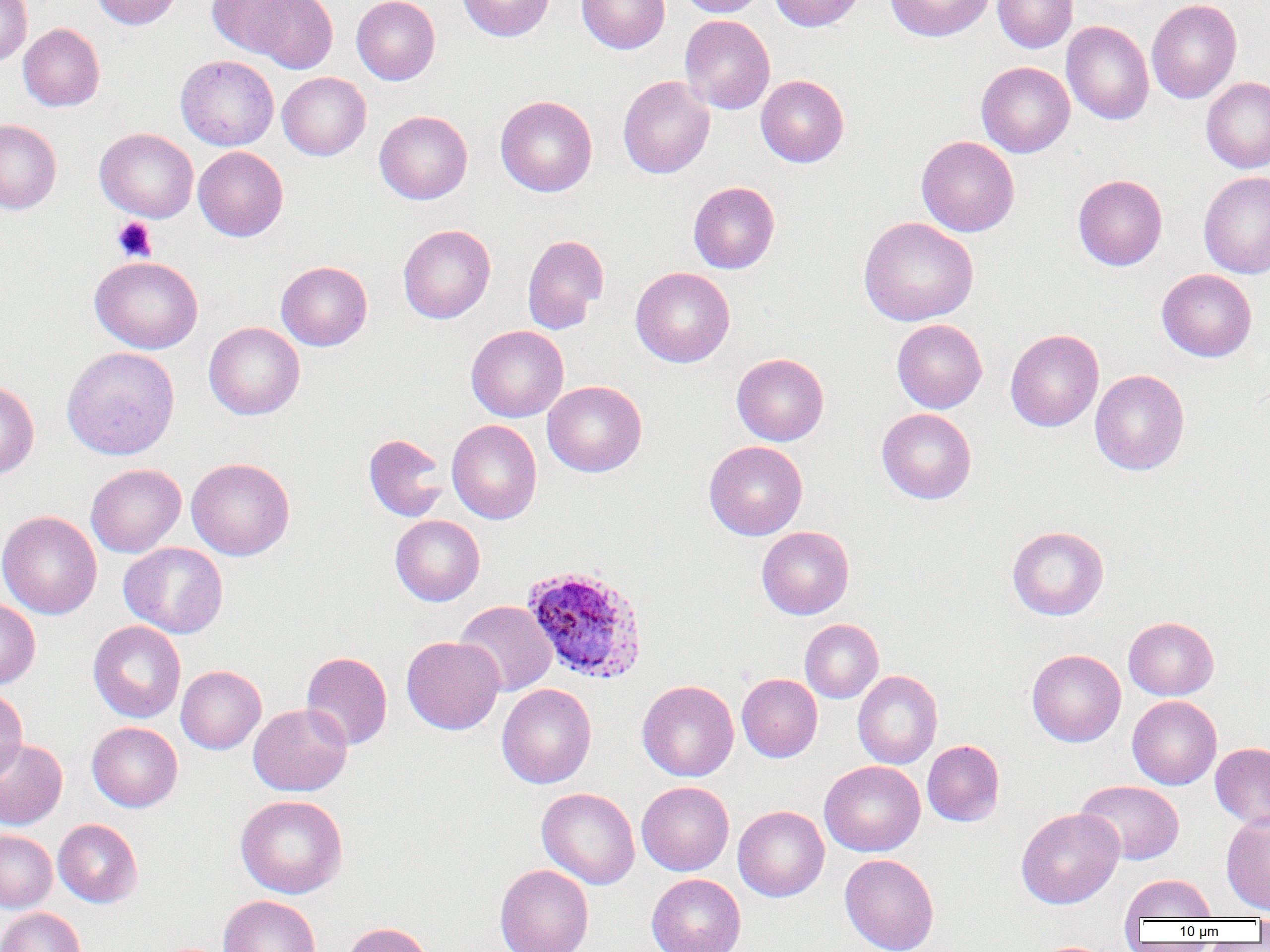
{
  "slide_level_diagnosis": "Plasmodium ovale",
  "preparation": "thin blood film",
  "plasmodium_ovale_infected_red_blood_cell_locations": "approximate bounding boxes as named x1/y1/x2/y2 corners in pixels: (x1=521, y1=564, x2=648, y2=684)",
  "magnification": "1000x",
  "platelet_locations": "approximate bounding boxes as named x1/y1/x2/y2 corners in pixels: (x1=112, y1=217, x2=157, y2=262)",
  "uninfected_red_blood_cell_locations": "approximate bounding boxes as named x1/y1/x2/y2 corners in pixels: (x1=0, y1=0, x2=32, y2=65), (x1=91, y1=0, x2=182, y2=29), (x1=206, y1=0, x2=302, y2=59), (x1=246, y1=0, x2=338, y2=74), (x1=352, y1=0, x2=440, y2=85), (x1=457, y1=0, x2=554, y2=41), (x1=576, y1=0, x2=669, y2=54), (x1=677, y1=0, x2=767, y2=17), (x1=768, y1=0, x2=866, y2=31), (x1=885, y1=0, x2=993, y2=42), (x1=993, y1=0, x2=1078, y2=53), (x1=1146, y1=0, x2=1242, y2=104), (x1=679, y1=15, x2=775, y2=114), (x1=1061, y1=20, x2=1154, y2=125), (x1=18, y1=23, x2=105, y2=111), (x1=175, y1=55, x2=279, y2=150), (x1=976, y1=61, x2=1075, y2=157), (x1=277, y1=72, x2=371, y2=160), (x1=756, y1=75, x2=849, y2=167), (x1=617, y1=76, x2=715, y2=178), (x1=1201, y1=77, x2=1270, y2=173), (x1=495, y1=95, x2=597, y2=197), (x1=375, y1=110, x2=473, y2=204), (x1=0, y1=119, x2=62, y2=214), (x1=95, y1=127, x2=198, y2=222), (x1=916, y1=136, x2=1020, y2=237), (x1=193, y1=146, x2=288, y2=241), (x1=1199, y1=171, x2=1270, y2=278), (x1=1073, y1=174, x2=1167, y2=270), (x1=688, y1=181, x2=780, y2=274), (x1=859, y1=216, x2=978, y2=326), (x1=398, y1=224, x2=496, y2=324), (x1=522, y1=234, x2=609, y2=334), (x1=89, y1=256, x2=203, y2=354), (x1=276, y1=261, x2=373, y2=350), (x1=631, y1=267, x2=735, y2=367), (x1=1156, y1=268, x2=1257, y2=362), (x1=892, y1=319, x2=987, y2=413), (x1=204, y1=321, x2=305, y2=420), (x1=466, y1=325, x2=569, y2=422), (x1=1005, y1=329, x2=1104, y2=432), (x1=61, y1=346, x2=180, y2=460), (x1=731, y1=353, x2=829, y2=446), (x1=1090, y1=369, x2=1189, y2=475), (x1=0, y1=380, x2=39, y2=480), (x1=542, y1=380, x2=647, y2=477), (x1=877, y1=408, x2=977, y2=504), (x1=447, y1=420, x2=542, y2=524), (x1=363, y1=433, x2=449, y2=522), (x1=704, y1=441, x2=807, y2=540), (x1=187, y1=457, x2=295, y2=560), (x1=86, y1=464, x2=186, y2=557), (x1=0, y1=511, x2=102, y2=619), (x1=390, y1=515, x2=485, y2=606), (x1=757, y1=526, x2=854, y2=619), (x1=1007, y1=526, x2=1109, y2=620), (x1=119, y1=542, x2=228, y2=638), (x1=0, y1=599, x2=41, y2=690), (x1=454, y1=600, x2=557, y2=696), (x1=1123, y1=617, x2=1219, y2=700), (x1=800, y1=619, x2=884, y2=703), (x1=88, y1=620, x2=186, y2=723), (x1=401, y1=635, x2=504, y2=734), (x1=1027, y1=649, x2=1126, y2=746), (x1=301, y1=651, x2=392, y2=750), (x1=176, y1=665, x2=266, y2=754), (x1=853, y1=670, x2=943, y2=769), (x1=737, y1=673, x2=822, y2=762), (x1=637, y1=680, x2=739, y2=781), (x1=496, y1=684, x2=597, y2=789), (x1=0, y1=687, x2=27, y2=783), (x1=1127, y1=695, x2=1222, y2=790), (x1=248, y1=703, x2=352, y2=796), (x1=87, y1=722, x2=183, y2=812), (x1=0, y1=738, x2=68, y2=829), (x1=922, y1=740, x2=1005, y2=827), (x1=1210, y1=742, x2=1270, y2=829), (x1=819, y1=761, x2=925, y2=856), (x1=1076, y1=779, x2=1184, y2=865), (x1=636, y1=781, x2=734, y2=876), (x1=537, y1=787, x2=640, y2=889), (x1=235, y1=794, x2=348, y2=899), (x1=636, y1=796, x2=828, y2=884), (x1=733, y1=805, x2=829, y2=902), (x1=1016, y1=807, x2=1124, y2=909), (x1=1221, y1=812, x2=1270, y2=915), (x1=53, y1=818, x2=143, y2=907), (x1=0, y1=829, x2=57, y2=913), (x1=840, y1=853, x2=939, y2=952), (x1=494, y1=863, x2=594, y2=952), (x1=646, y1=874, x2=745, y2=952), (x1=1120, y1=874, x2=1217, y2=923), (x1=219, y1=895, x2=320, y2=952), (x1=0, y1=907, x2=85, y2=952), (x1=1254, y1=913, x2=1270, y2=941), (x1=341, y1=922, x2=433, y2=952)",
  "field_of_view": "one of a larger specimen",
  "modality": "optical microscopy",
  "image_size": "1270×952 pixels"
}